Identify the parasite.
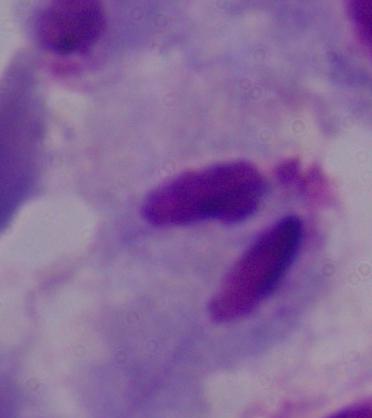

A trichomonad.

Micrograph. Captured at 1000x magnification.